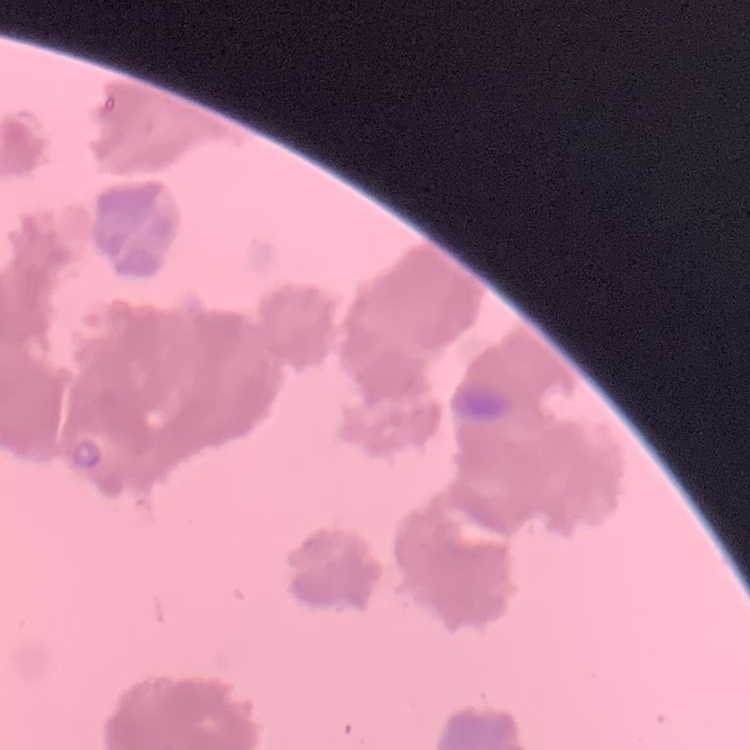

red blood cell morphology = rouleaux formation
image type = square crop of a larger photomicrograph
stain = Field's or Giemsa
preparation = thin peripheral smear